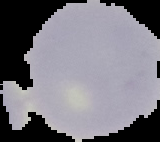
result = negative for malaria parasites
image type = cell region segmented out of the field of view; surrounding area masked to black
preparation = thin blood film
image size = 160×142 pixels